Report the malaria status of this cell.
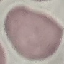
Uninfected.

image type = automatically extracted cell patch, resized to 64 × 64 pixels
capture = smartphone through the microscope eyepiece
preparation = thin smear
stain = Giemsa